Identify the blood parasite species.
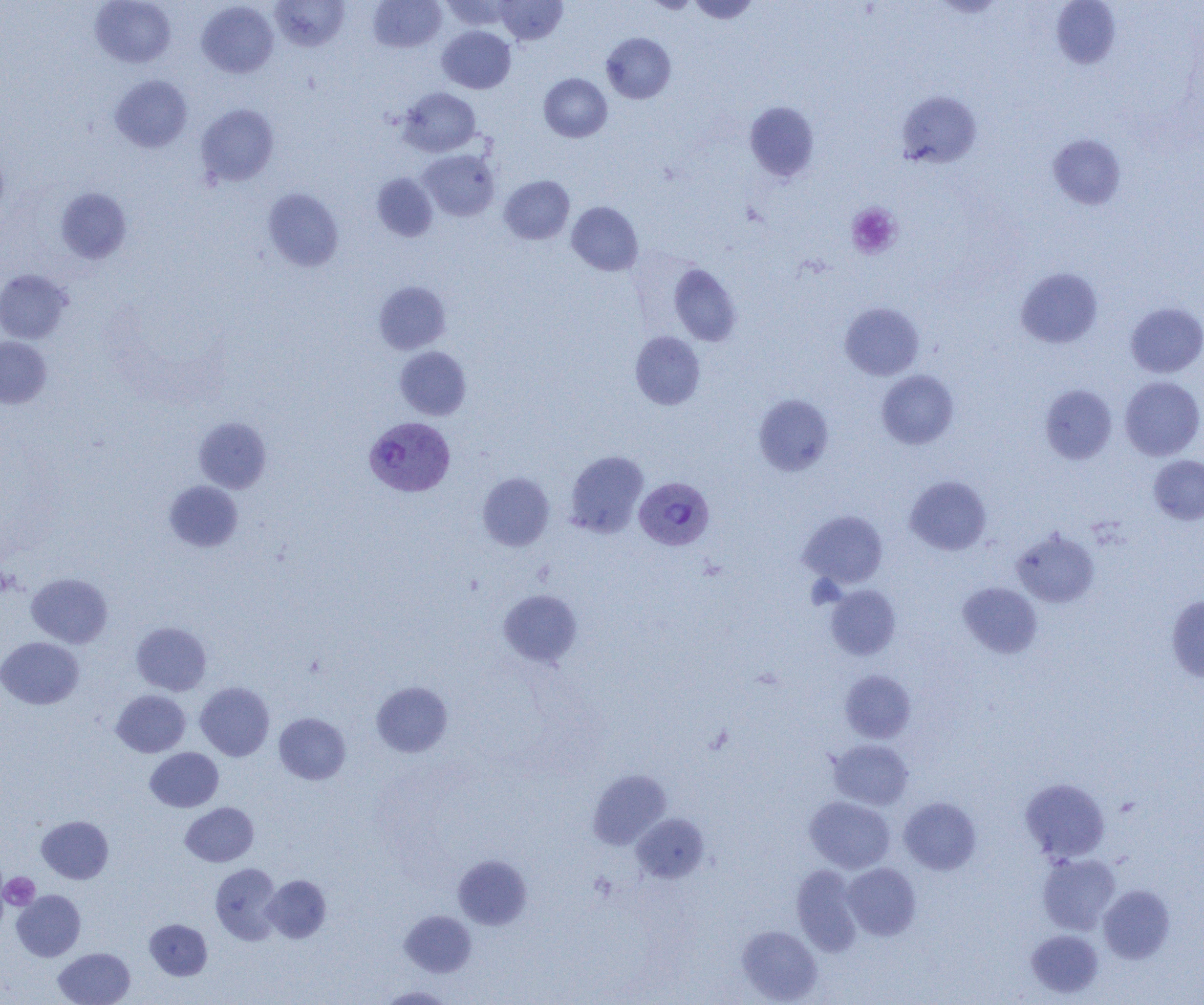

Plasmodium vivax.

{
  "platelet_locations": "approximate bounding boxes as named x1/y1/x2/y2 corners in pixels: (x1=846, y1=203, x2=901, y2=259), (x1=806, y1=575, x2=844, y2=609), (x1=1, y1=872, x2=40, y2=911)",
  "uninfected_red_blood_cell_locations": "approximate bounding boxes as named x1/y1/x2/y2 corners in pixels: (x1=90, y1=0, x2=176, y2=68), (x1=270, y1=0, x2=350, y2=52), (x1=367, y1=0, x2=446, y2=53), (x1=440, y1=0, x2=516, y2=30), (x1=495, y1=0, x2=567, y2=45), (x1=643, y1=0, x2=700, y2=13), (x1=687, y1=0, x2=760, y2=24), (x1=197, y1=1, x2=278, y2=78), (x1=1051, y1=1, x2=1121, y2=69), (x1=438, y1=26, x2=516, y2=93), (x1=601, y1=33, x2=676, y2=104), (x1=539, y1=73, x2=612, y2=142), (x1=110, y1=75, x2=192, y2=153), (x1=398, y1=87, x2=481, y2=156), (x1=896, y1=91, x2=982, y2=168), (x1=744, y1=101, x2=819, y2=181), (x1=196, y1=104, x2=278, y2=187), (x1=1048, y1=134, x2=1126, y2=210), (x1=419, y1=149, x2=499, y2=221), (x1=371, y1=173, x2=438, y2=241), (x1=500, y1=175, x2=574, y2=244), (x1=55, y1=188, x2=131, y2=263), (x1=262, y1=188, x2=343, y2=271), (x1=567, y1=201, x2=643, y2=275), (x1=668, y1=262, x2=742, y2=347), (x1=1016, y1=267, x2=1102, y2=348), (x1=0, y1=269, x2=72, y2=344), (x1=374, y1=281, x2=451, y2=354), (x1=840, y1=301, x2=924, y2=380), (x1=1125, y1=302, x2=1204, y2=378), (x1=630, y1=331, x2=705, y2=410), (x1=0, y1=336, x2=51, y2=408), (x1=394, y1=346, x2=471, y2=420), (x1=876, y1=370, x2=959, y2=449), (x1=1120, y1=376, x2=1204, y2=460), (x1=1040, y1=384, x2=1117, y2=465), (x1=752, y1=394, x2=833, y2=476), (x1=194, y1=417, x2=271, y2=493), (x1=564, y1=451, x2=648, y2=537), (x1=1148, y1=455, x2=1204, y2=525), (x1=477, y1=472, x2=555, y2=551), (x1=905, y1=475, x2=992, y2=555), (x1=164, y1=481, x2=242, y2=551), (x1=798, y1=510, x2=888, y2=588), (x1=1012, y1=528, x2=1100, y2=608), (x1=26, y1=573, x2=113, y2=648), (x1=958, y1=582, x2=1042, y2=658), (x1=826, y1=585, x2=901, y2=660), (x1=498, y1=589, x2=582, y2=668), (x1=1166, y1=594, x2=1204, y2=683), (x1=131, y1=622, x2=211, y2=695), (x1=0, y1=637, x2=84, y2=708), (x1=840, y1=670, x2=915, y2=743), (x1=371, y1=681, x2=453, y2=757), (x1=195, y1=682, x2=274, y2=761), (x1=112, y1=690, x2=190, y2=757), (x1=274, y1=712, x2=350, y2=784), (x1=829, y1=740, x2=913, y2=809), (x1=145, y1=747, x2=223, y2=812), (x1=588, y1=769, x2=670, y2=849), (x1=1019, y1=777, x2=1110, y2=863), (x1=805, y1=796, x2=895, y2=873), (x1=899, y1=797, x2=981, y2=875), (x1=180, y1=802, x2=258, y2=866), (x1=632, y1=814, x2=708, y2=882), (x1=36, y1=816, x2=113, y2=883), (x1=1037, y1=852, x2=1120, y2=935), (x1=453, y1=855, x2=532, y2=929), (x1=210, y1=863, x2=282, y2=944), (x1=842, y1=863, x2=920, y2=940), (x1=791, y1=865, x2=863, y2=956), (x1=262, y1=875, x2=331, y2=942), (x1=1098, y1=885, x2=1175, y2=964), (x1=12, y1=890, x2=85, y2=961), (x1=400, y1=910, x2=476, y2=977), (x1=145, y1=919, x2=212, y2=979), (x1=737, y1=925, x2=822, y2=1003), (x1=1026, y1=929, x2=1103, y2=998), (x1=54, y1=947, x2=135, y2=1005), (x1=377, y1=986, x2=454, y2=1004)",
  "modality": "optical microscopy",
  "magnification": "1000x",
  "image_size": "1204×1005 pixels",
  "plasmodium_vivax_infected_red_blood_cell_locations": "approximate bounding boxes as named x1/y1/x2/y2 corners in pixels: (x1=365, y1=417, x2=454, y2=497), (x1=635, y1=477, x2=714, y2=550)",
  "field_of_view": "single",
  "preparation": "thin blood smear"
}